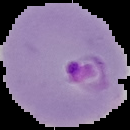
Summary:
  - Preparation: thin blood film
  - Image size: 130×130 pixels
  - Malaria status: parasitized
  - Image type: segmented cell region on a black background